Classify this cell by malaria status.
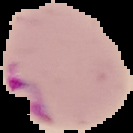
Parasitized.

Cell region segmented out of the field of view; the surrounding area is masked to black. Image is 133×133 pixels. From a thin blood film.